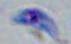
modality: photomicrograph
magnification: 1000x
identification: Toxoplasma gondii